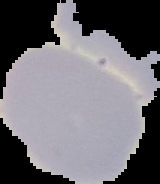

result = negative for malaria parasites
image type = cell region segmented out of the field of view; surrounding area masked to black
image size = 160×184 pixels
preparation = thin blood smear